Locate every leukocyte (white blood cell).
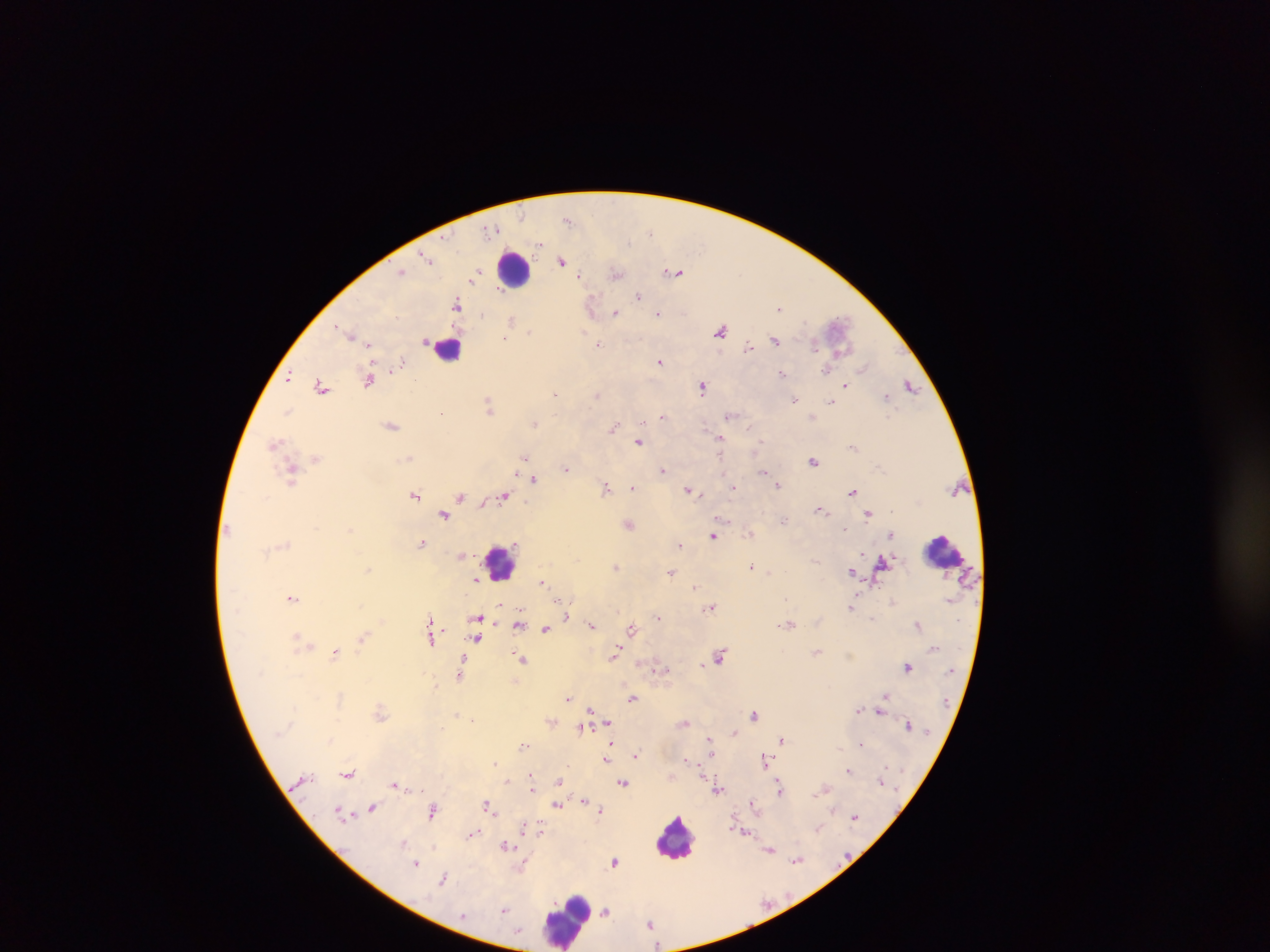
Approximate centers as {x, y} in pixels.
Leukocytes: {514, 269}, {448, 348}, {943, 551}, {502, 562}, {676, 837}, {566, 919}.

Summary:
  - Malaria parasite locations: {567, 220}, {492, 230}, {650, 232}, {540, 244}, {425, 256}, {428, 259}, {562, 261}, {401, 271}, {674, 272}, {616, 273}, {475, 275}, {579, 275}, {473, 280}, {639, 296}, {457, 303}, {592, 306}, {779, 309}, {616, 313}, {659, 313}, {511, 320}, {530, 331}, {721, 331}, {583, 333}, {349, 334}, {505, 338}, {775, 340}, {369, 344}, {599, 345}, {814, 345}, {748, 347}, {403, 362}, {660, 362}, {863, 366}, {826, 370}, {782, 373}, {289, 377}, {414, 379}, {369, 380}, {846, 384}, {321, 386}, {910, 386}, {703, 388}, {555, 394}, {597, 394}, {886, 396}, {795, 400}, {830, 401}, {489, 407}, {287, 410}, {441, 412}, {730, 415}, {663, 416}, {642, 421}, {534, 424}, {392, 426}, {614, 427}, {750, 428}, {721, 439}, {761, 440}, {275, 442}, {639, 442}, {854, 447}, {524, 456}, {409, 458}, {316, 459}, {814, 462}, {877, 466}, {565, 468}, {663, 470}, {764, 472}, {516, 473}, {292, 474}, {725, 474}, {534, 478}, {778, 485}, {606, 487}, {633, 487}, {688, 489}, {734, 489}, {853, 491}, {416, 495}, {460, 496}, {503, 496}, {483, 503}, {821, 508}, {444, 513}, {869, 514}, {723, 520}, {784, 520}, {629, 524}, {844, 529}, {750, 533}, {890, 535}, {713, 536}, {422, 543}, {680, 545}, {861, 552}, {814, 560}, {883, 561}, {752, 565}, {617, 566}, {368, 569}, {851, 571}, {672, 572}, {770, 573}, {476, 580}, {541, 582}, {695, 586}, {292, 597}, {562, 602}, {500, 604}, {711, 606}, {852, 606}, {568, 616}, {659, 617}, {478, 618}, {871, 618}, {430, 619}, {519, 624}, {790, 624}, {918, 624}, {592, 626}, {545, 629}, {632, 629}, {296, 637}, {362, 637}, {477, 638}, {432, 639}, {304, 642}, {310, 646}, {817, 651}, {335, 653}, {615, 653}, {721, 655}, {521, 659}, {703, 664}, {907, 667}, {657, 668}, {460, 675}, {885, 696}, {633, 698}, {569, 699}, {883, 701}, {591, 709}, {858, 709}, {880, 710}, {380, 712}, {457, 714}, {754, 715}, {473, 719}, {609, 722}, {686, 723}, {907, 724}, {581, 727}, {734, 732}, {710, 739}, {781, 740}, {331, 741}, {861, 743}, {611, 744}, {523, 745}, {840, 749}, {636, 755}, {711, 755}, {686, 758}, {764, 758}, {606, 759}, {495, 763}, {848, 770}, {348, 773}, {531, 775}, {881, 780}, {507, 781}, {558, 782}, {623, 783}, {395, 785}, {779, 787}, {533, 789}, {718, 789}, {818, 793}, {585, 801}, {753, 802}, {487, 805}, {557, 805}, {372, 808}, {600, 810}, {339, 811}, {433, 811}, {855, 817}, {523, 829}, {819, 829}, {540, 831}, {745, 832}, {473, 834}, {404, 842}, {506, 846}, {770, 849}, {796, 860}, {615, 861}, {416, 863}, {522, 867}, {444, 878}, {505, 910}, {606, 911}, {650, 923}
  - Country: Ghana
  - Capture: mobile-phone photograph through a microscope
  - Field of view: single
  - Image size: 1270×952 pixels
  - Preparation: thick blood smear